Classify this cell by malaria status.
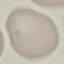
It is uninfected.

Summary:
  - Stain: Giemsa
  - Capture: smartphone through the microscope eyepiece
  - Preparation: thin blood film
  - Image type: automatically extracted cell patch, resized to 64 × 64 pixels